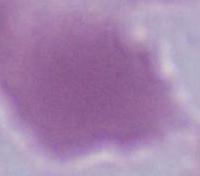

identification = erythrocyte
modality = micrograph
magnification = 1000x